Classify this cell by malaria status.
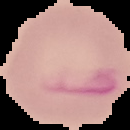

Uninfected.

The area outside the segmented cell region is set to black. Image is 130×130 pixels. From a thin blood smear.